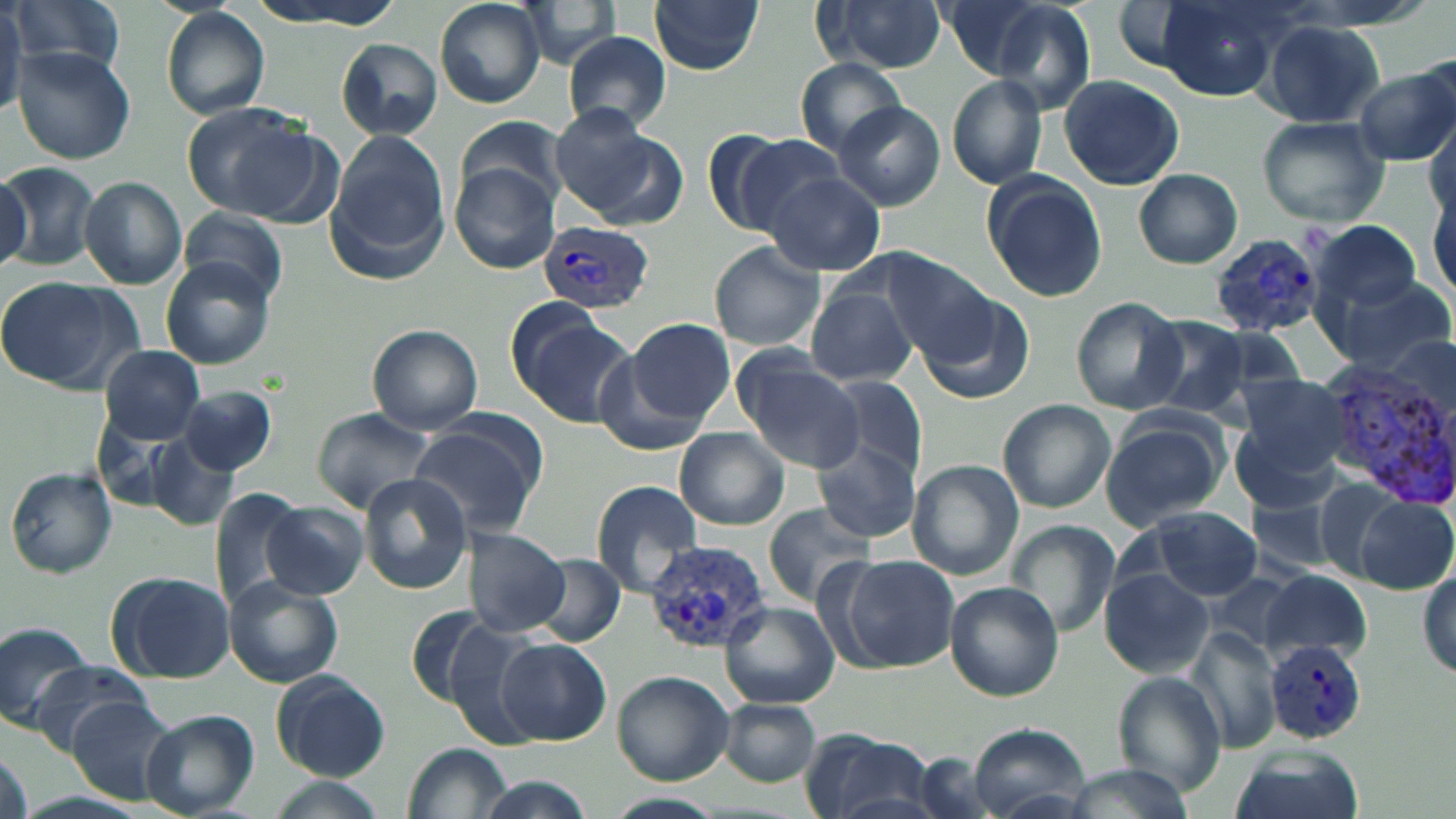

Summary:
  - Coordinate format: approximate bounding boxes as named x1/y1/x2/y2 corners in pixels
  - Uninfected red blood cell locations: (x1=0, y1=0, x2=25, y2=117), (x1=9, y1=0, x2=127, y2=77), (x1=243, y1=0, x2=406, y2=29), (x1=434, y1=0, x2=547, y2=108), (x1=513, y1=0, x2=626, y2=68), (x1=940, y1=0, x2=1068, y2=82), (x1=1151, y1=0, x2=1289, y2=101), (x1=648, y1=1, x2=765, y2=74), (x1=811, y1=1, x2=949, y2=74), (x1=162, y1=8, x2=271, y2=120), (x1=1261, y1=20, x2=1386, y2=128), (x1=564, y1=31, x2=673, y2=133), (x1=336, y1=39, x2=442, y2=141), (x1=12, y1=48, x2=136, y2=164), (x1=794, y1=57, x2=908, y2=157), (x1=1356, y1=67, x2=1456, y2=166), (x1=947, y1=73, x2=1050, y2=191), (x1=1057, y1=74, x2=1187, y2=189), (x1=834, y1=102, x2=945, y2=211), (x1=180, y1=103, x2=316, y2=217), (x1=1428, y1=111, x2=1456, y2=226), (x1=554, y1=114, x2=686, y2=231), (x1=1256, y1=116, x2=1389, y2=228), (x1=457, y1=120, x2=566, y2=209), (x1=720, y1=132, x2=843, y2=237), (x1=326, y1=134, x2=448, y2=276), (x1=0, y1=161, x2=100, y2=271), (x1=451, y1=164, x2=557, y2=273), (x1=1134, y1=169, x2=1243, y2=268), (x1=0, y1=170, x2=31, y2=271), (x1=982, y1=172, x2=1108, y2=301), (x1=765, y1=173, x2=885, y2=276), (x1=80, y1=177, x2=187, y2=289), (x1=1429, y1=182, x2=1455, y2=301), (x1=178, y1=208, x2=288, y2=306), (x1=1311, y1=219, x2=1422, y2=313), (x1=709, y1=242, x2=825, y2=353), (x1=881, y1=253, x2=1004, y2=365), (x1=160, y1=257, x2=276, y2=370), (x1=0, y1=275, x2=141, y2=392), (x1=1326, y1=275, x2=1453, y2=375), (x1=805, y1=287, x2=918, y2=388), (x1=919, y1=292, x2=1035, y2=406), (x1=1070, y1=297, x2=1188, y2=414), (x1=509, y1=308, x2=632, y2=423), (x1=1141, y1=315, x2=1250, y2=418), (x1=627, y1=317, x2=734, y2=423), (x1=368, y1=324, x2=484, y2=433), (x1=99, y1=345, x2=206, y2=444), (x1=591, y1=348, x2=715, y2=457), (x1=734, y1=354, x2=865, y2=472), (x1=1234, y1=372, x2=1352, y2=479), (x1=819, y1=374, x2=930, y2=486), (x1=179, y1=384, x2=276, y2=475), (x1=997, y1=399, x2=1116, y2=513), (x1=313, y1=408, x2=434, y2=511), (x1=1099, y1=415, x2=1229, y2=532), (x1=408, y1=416, x2=545, y2=533), (x1=1231, y1=423, x2=1338, y2=515), (x1=673, y1=427, x2=791, y2=531), (x1=815, y1=436, x2=921, y2=543), (x1=151, y1=437, x2=242, y2=531), (x1=907, y1=461, x2=1024, y2=579), (x1=6, y1=467, x2=117, y2=578), (x1=358, y1=474, x2=472, y2=594), (x1=1309, y1=476, x2=1411, y2=579), (x1=589, y1=481, x2=703, y2=597), (x1=209, y1=488, x2=311, y2=617), (x1=1245, y1=493, x2=1347, y2=576), (x1=1356, y1=494, x2=1455, y2=593), (x1=263, y1=503, x2=368, y2=600), (x1=762, y1=505, x2=877, y2=605), (x1=1143, y1=508, x2=1263, y2=600), (x1=1008, y1=521, x2=1119, y2=635), (x1=460, y1=524, x2=570, y2=638), (x1=530, y1=554, x2=625, y2=648), (x1=845, y1=556, x2=958, y2=671), (x1=1417, y1=568, x2=1455, y2=683), (x1=1099, y1=569, x2=1213, y2=677), (x1=1259, y1=569, x2=1371, y2=662), (x1=108, y1=571, x2=234, y2=683), (x1=1210, y1=573, x2=1306, y2=655), (x1=224, y1=576, x2=343, y2=688), (x1=946, y1=582, x2=1064, y2=701), (x1=721, y1=600, x2=839, y2=707), (x1=403, y1=606, x2=505, y2=710), (x1=0, y1=617, x2=91, y2=728), (x1=433, y1=617, x2=549, y2=753), (x1=1189, y1=625, x2=1282, y2=751), (x1=497, y1=638, x2=610, y2=744), (x1=27, y1=661, x2=154, y2=753), (x1=1113, y1=670, x2=1227, y2=797), (x1=271, y1=671, x2=390, y2=780), (x1=612, y1=671, x2=735, y2=786), (x1=67, y1=697, x2=181, y2=803), (x1=715, y1=699, x2=821, y2=787), (x1=138, y1=710, x2=258, y2=818), (x1=965, y1=724, x2=1090, y2=816), (x1=799, y1=731, x2=943, y2=819), (x1=0, y1=740, x2=33, y2=819), (x1=404, y1=740, x2=511, y2=818), (x1=1229, y1=747, x2=1364, y2=819), (x1=913, y1=753, x2=1004, y2=819), (x1=1060, y1=764, x2=1199, y2=819), (x1=468, y1=775, x2=597, y2=818), (x1=265, y1=777, x2=388, y2=819), (x1=608, y1=792, x2=723, y2=817)
  - Plasmodium vivax-infected red blood cell locations: (x1=536, y1=221, x2=659, y2=313), (x1=1210, y1=229, x2=1329, y2=336), (x1=1318, y1=364, x2=1456, y2=505), (x1=644, y1=540, x2=776, y2=651), (x1=1268, y1=639, x2=1368, y2=745)
  - Slide-level diagnosis: Plasmodium vivax
  - Preparation: thin blood smear
  - Modality: light microscopy
  - Image size: 1456×819 pixels
  - Magnification: 1000x
  - Stain: May-Grünwald-Giemsa
  - Field of view: single